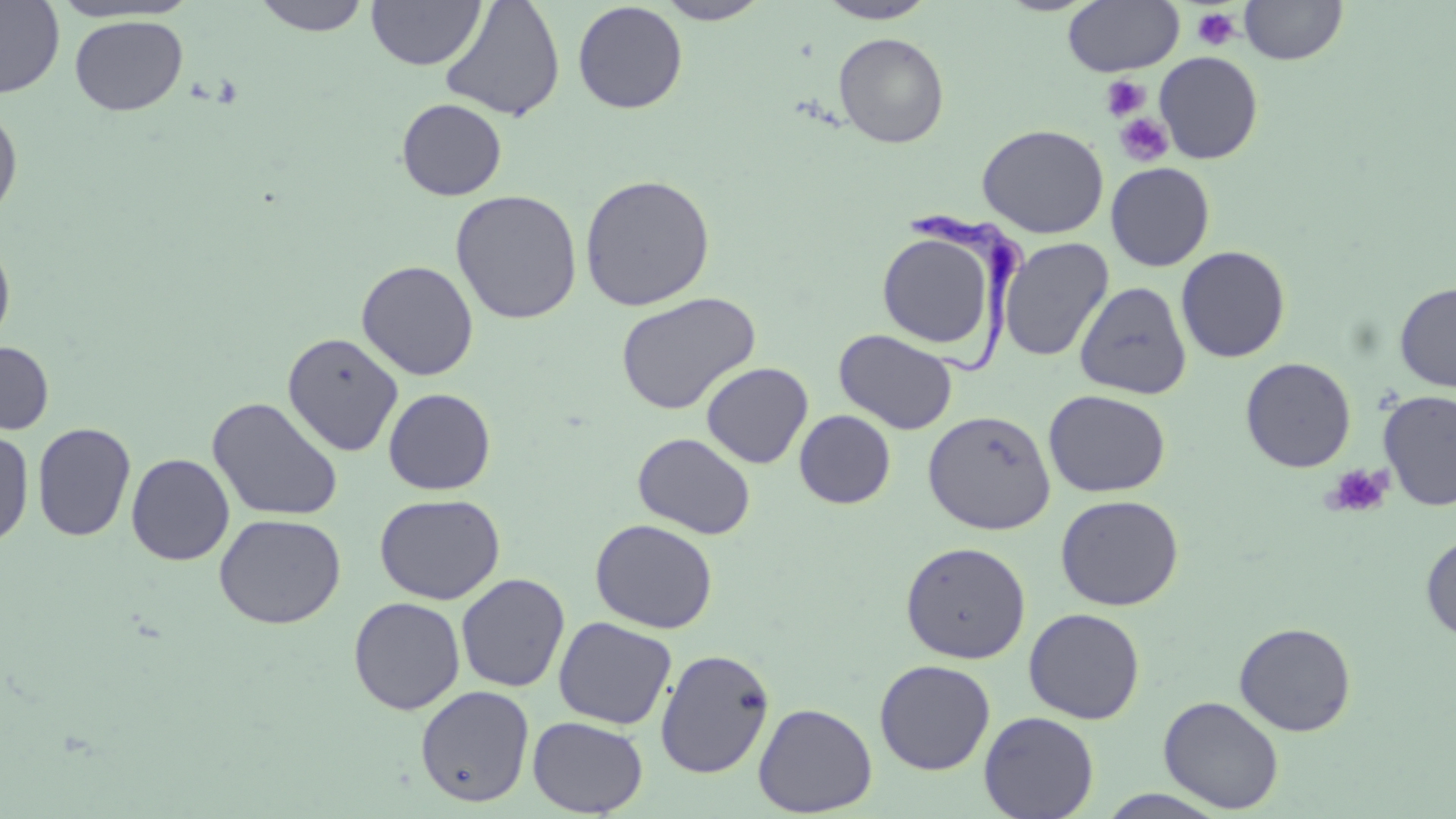 Approximate bounding boxes as [x1, y1, x2, y2] in pixels. Uninfected red blood cell locations: [0, 0, 65, 99], [251, 0, 371, 36], [366, 0, 485, 70], [440, 0, 566, 122], [655, 0, 772, 24], [817, 0, 938, 24], [1240, 0, 1347, 65], [1063, 1, 1184, 76], [572, 2, 688, 114], [69, 15, 188, 116], [833, 32, 949, 148], [1154, 51, 1263, 164], [397, 98, 507, 201], [0, 106, 23, 221], [976, 124, 1109, 238], [1106, 162, 1215, 271], [579, 173, 715, 311], [450, 189, 582, 324], [876, 231, 1000, 352], [0, 237, 16, 353], [998, 237, 1114, 362], [1175, 245, 1291, 363], [356, 260, 479, 381], [1074, 281, 1193, 400], [1395, 282, 1456, 391], [615, 292, 761, 415], [835, 329, 958, 435], [281, 331, 404, 456], [0, 341, 54, 434], [1240, 357, 1356, 473], [701, 362, 813, 469], [383, 388, 496, 495], [1043, 389, 1170, 497], [1378, 390, 1456, 511], [207, 397, 344, 522], [795, 410, 896, 509], [923, 410, 1056, 535], [32, 422, 136, 542], [0, 427, 34, 548], [632, 432, 756, 539], [126, 453, 234, 565], [375, 493, 505, 604], [1055, 494, 1183, 611], [214, 513, 346, 629], [590, 518, 718, 633], [1420, 533, 1456, 643], [900, 540, 1031, 664], [456, 573, 571, 693], [348, 597, 465, 715], [1023, 608, 1145, 724], [553, 617, 677, 730], [1234, 622, 1356, 736], [655, 648, 775, 779], [874, 659, 995, 775], [415, 685, 535, 807], [1158, 695, 1285, 813], [753, 702, 878, 816], [979, 711, 1099, 819], [527, 716, 648, 817], [1096, 789, 1231, 818]. Trypanosoma brucei locations: [909, 207, 1031, 377]. Platelet locations: [1192, 7, 1241, 51], [1101, 75, 1150, 120], [1114, 113, 1174, 167], [1323, 464, 1394, 518]. Slide-level diagnosis: Trypanosoma brucei. Image is 1456×819 pixels. Thin blood film. 1000x magnification. May-Grünwald-Giemsa-stained preparation. Light microscopy. Single field of view.